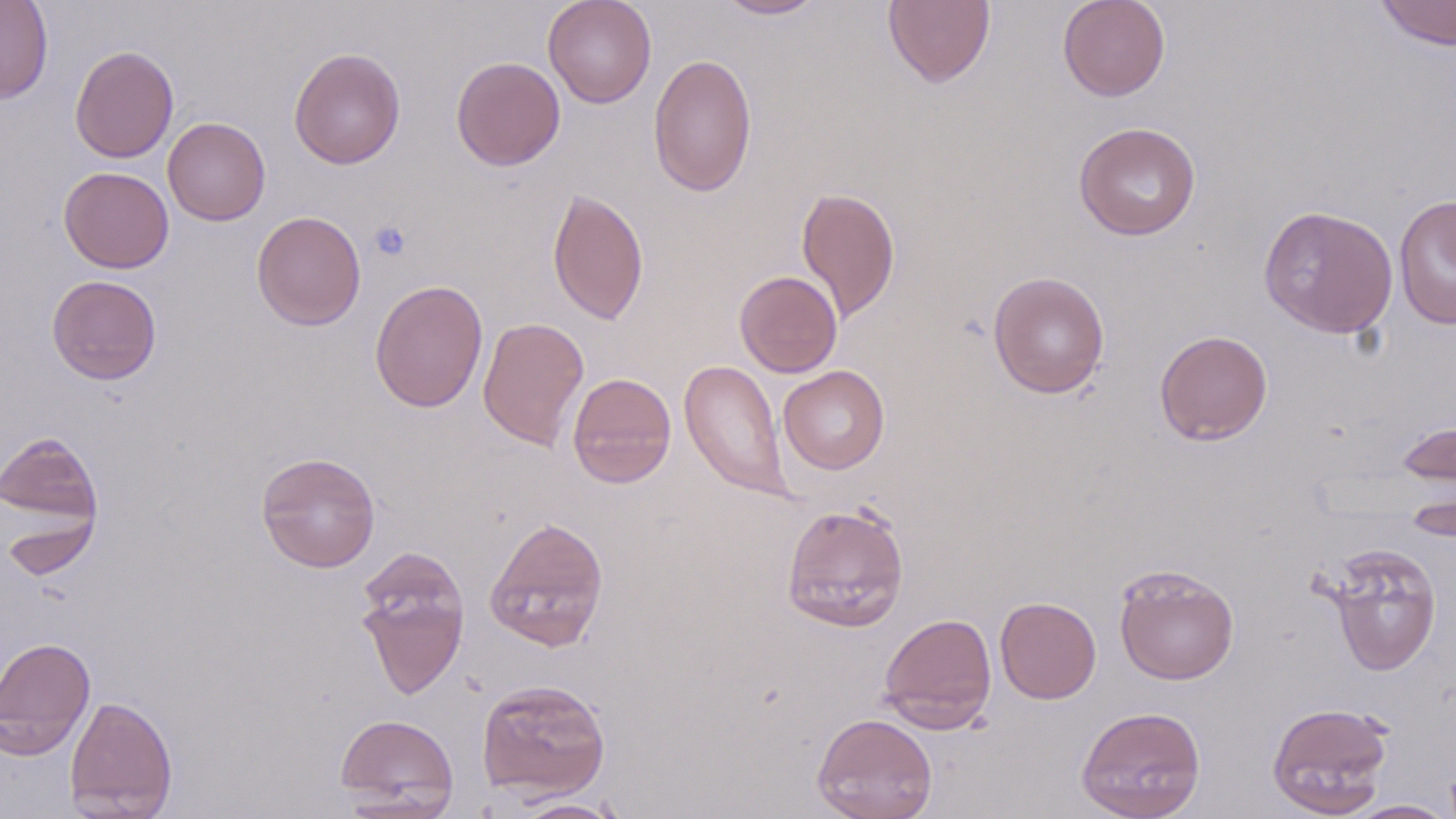

Approximate bounding boxes as [x1, y1, x2, y2] in pixels. Platelet locations: [369, 220, 412, 261]. Uninfected red blood cell locations: [0, 0, 54, 103], [542, 0, 657, 108], [714, 0, 827, 20], [882, 0, 996, 88], [1057, 0, 1171, 102], [1374, 0, 1456, 51], [70, 45, 178, 163], [288, 47, 406, 169], [648, 52, 757, 197], [451, 56, 566, 171], [163, 117, 271, 225], [1073, 121, 1201, 241], [58, 166, 174, 273], [796, 186, 900, 322], [547, 188, 648, 325], [1393, 194, 1456, 329], [1258, 205, 1398, 338], [251, 210, 366, 331], [734, 270, 843, 378], [987, 270, 1110, 399], [46, 275, 162, 384], [369, 279, 488, 413], [477, 317, 590, 451], [1154, 329, 1273, 445], [679, 358, 793, 504], [779, 366, 890, 474], [567, 372, 677, 488], [1396, 416, 1456, 493], [0, 430, 103, 529], [256, 451, 380, 573], [1402, 489, 1455, 543], [781, 501, 910, 633], [0, 506, 100, 581], [484, 515, 609, 652], [1323, 542, 1443, 677], [354, 546, 471, 702], [1113, 563, 1239, 684], [994, 596, 1102, 704], [878, 612, 997, 733], [0, 636, 96, 758], [476, 679, 611, 800], [64, 695, 178, 818], [1267, 701, 1394, 816], [1075, 705, 1206, 819], [334, 713, 459, 813], [812, 713, 938, 819], [508, 797, 627, 818], [1346, 800, 1456, 818]. Slide-level diagnosis: no evidence of blood parasites. Thin blood smear. Single field of view. Optical microscopy. Captured at 1000x magnification. Image is 1456×819 pixels. May-Grünwald-Giemsa-stained preparation.